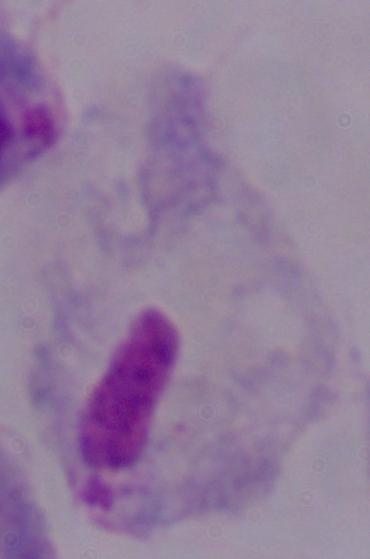 Micrograph. A trichomonad is shown. 1000x magnification.